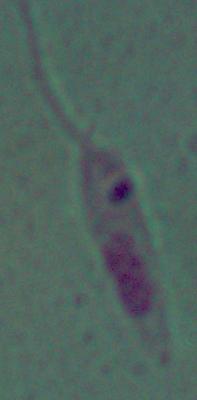
modality: photomicrograph
identification: Leishmania
magnification: 1000x